State the blood parasite species.
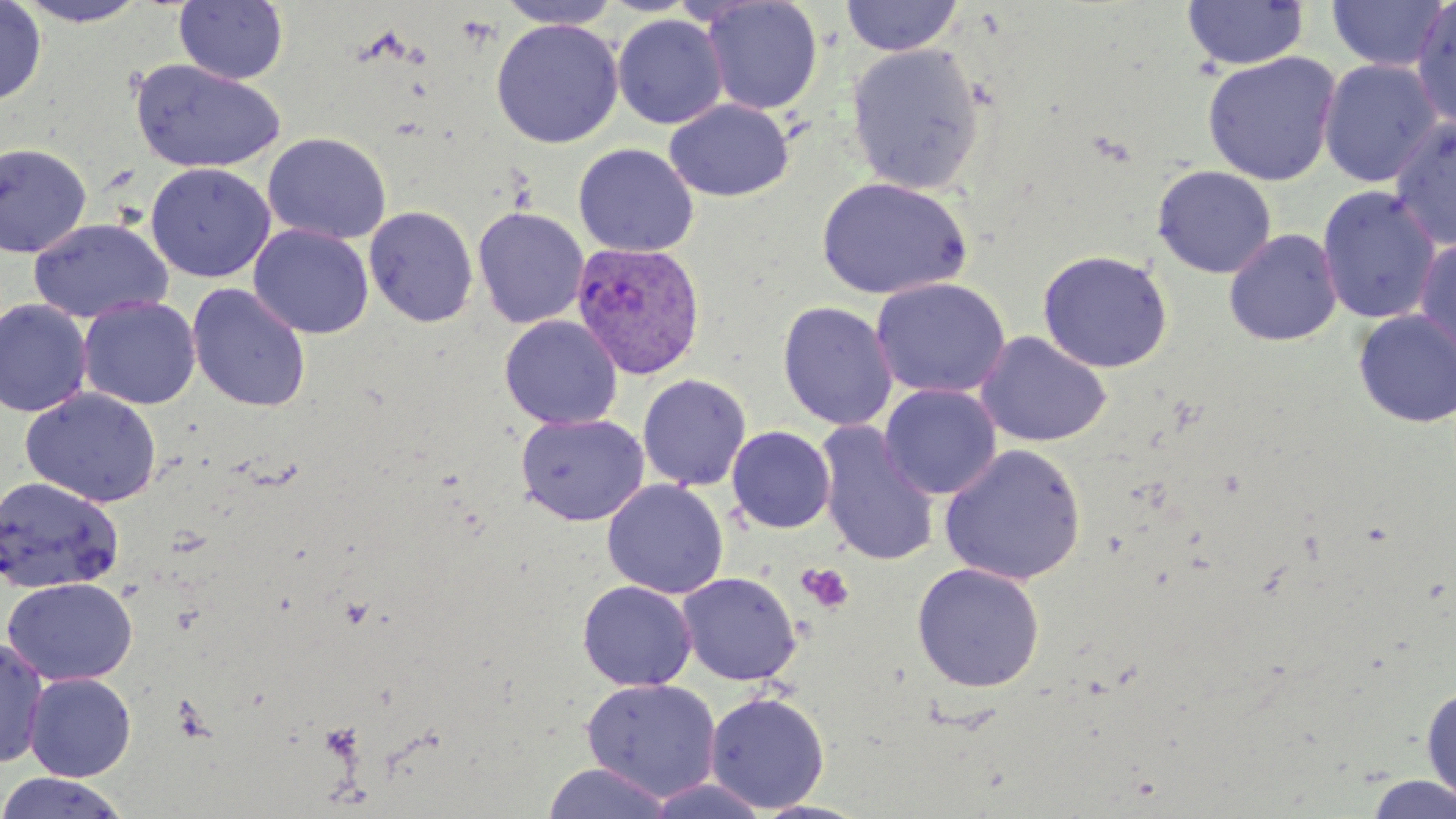
Plasmodium vivax.

stain = May-Grünwald-Giemsa
preparation = thin blood film
uninfected red blood cell locations = approximate bounding boxes as (x1,y1)-(x2,y2) corner pairs in pixels: (0,0)-(46,106), (174,0)-(289,85), (495,0)-(623,29), (840,0)-(963,57), (1181,0)-(1309,72), (1326,0)-(1452,72), (13,1)-(150,26), (700,1)-(823,116), (1411,1)-(1456,130), (612,14)-(728,129), (491,18)-(623,148), (846,43)-(985,195), (1202,51)-(1342,186), (1318,58)-(1444,188), (129,59)-(286,174), (664,99)-(794,202), (1389,115)-(1456,251), (263,132)-(392,245), (0,142)-(92,258), (573,143)-(698,257), (146,163)-(275,282), (1152,165)-(1277,279), (815,176)-(974,300), (1316,186)-(1443,325), (364,206)-(479,328), (473,207)-(589,329), (28,218)-(173,324), (249,224)-(373,339), (1223,227)-(1344,347), (1414,237)-(1456,364), (1037,249)-(1173,373), (871,277)-(1012,399), (187,283)-(311,413), (79,296)-(201,410), (0,299)-(92,417), (778,301)-(898,431), (1351,309)-(1456,428), (499,315)-(622,430), (975,331)-(1112,448), (637,374)-(752,492), (879,384)-(1001,500), (20,389)-(163,507), (515,413)-(649,527), (815,422)-(941,567), (727,425)-(836,533), (939,443)-(1087,586), (0,476)-(123,594), (602,479)-(728,599), (911,562)-(1045,693), (678,572)-(801,685), (2,578)-(138,686), (577,580)-(697,691), (0,638)-(50,770), (24,673)-(136,782), (580,678)-(722,802), (1421,683)-(1456,805), (704,691)-(830,812), (541,762)-(675,819), (0,772)-(129,818), (1362,774)-(1456,818), (643,778)-(771,818), (753,800)-(871,819)
modality = light microscopy
platelet locations = approximate bounding boxes as (x1,y1)-(x2,y2) corner pairs in pixels: (797,563)-(854,615)
Plasmodium vivax-infected red blood cell locations = approximate bounding boxes as (x1,y1)-(x2,y2) corner pairs in pixels: (571,241)-(706,379)
field of view = one of a larger specimen
magnification = 1000x
image size = 1456×819 pixels